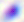
Summary:
  - Magnification: 400x
  - Modality: photomicrograph
  - Identification: Toxoplasma gondii